Classify this cell by malaria status.
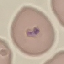
It is parasitized.

{
  "image_type": "automatically extracted cell patch, resized to 64 × 64 pixels",
  "preparation": "thin smear",
  "capture": "smartphone camera at the microscope eyepiece",
  "stain": "Giemsa"
}